Comment on the morphology of the red blood cells.
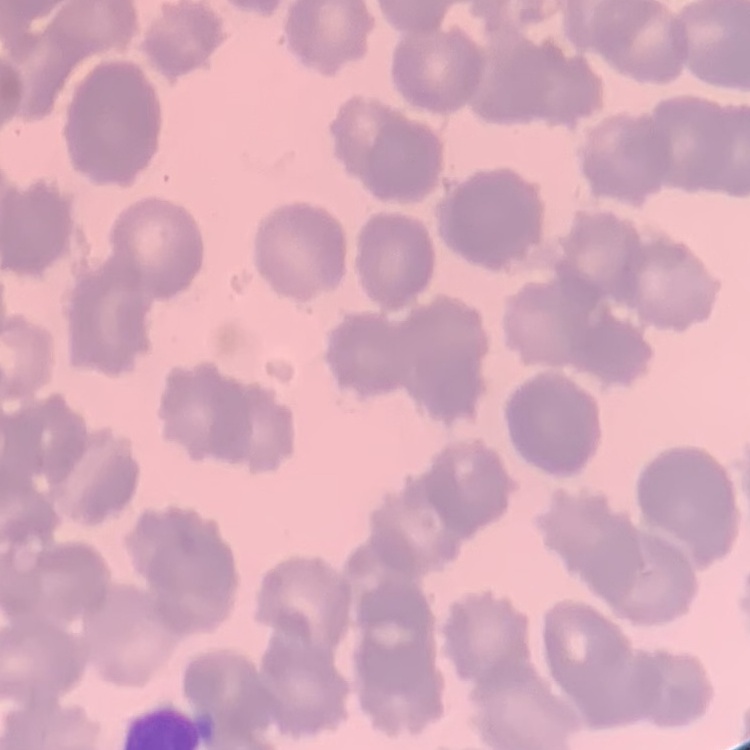

Rouleaux formation.

stain = Field's or Giemsa
image type = one tile cut from a larger photomicrograph
preparation = thin blood film